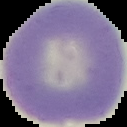

Summary:
  - Image size: 127×127 pixels
  - Image type: segmented cell region on a black background
  - Preparation: thin blood smear
  - Result: negative for malaria parasites